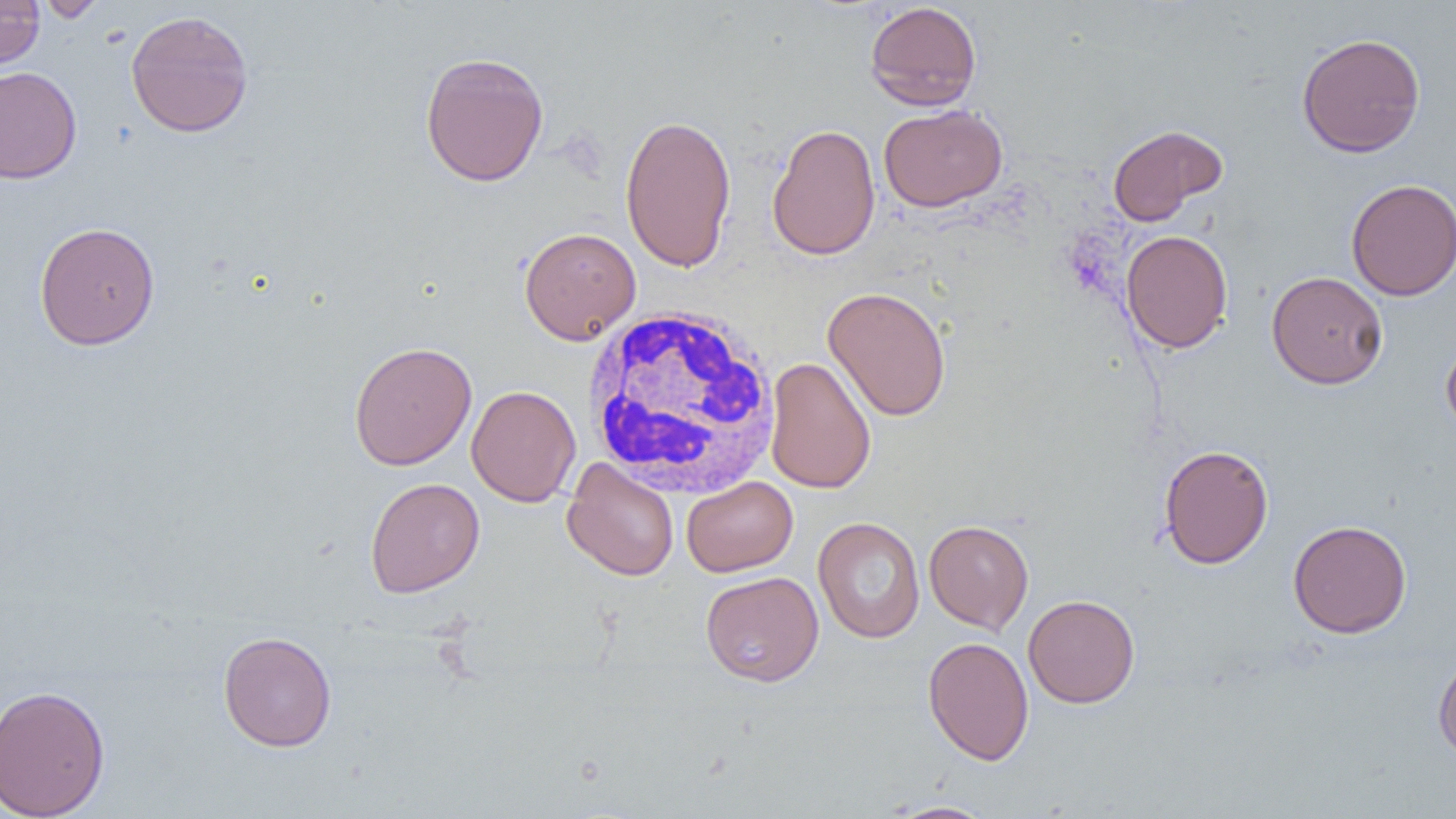
Summary:
  - Coordinate format: approximate bounding boxes as named x1/y1/x2/y2 corners in pixels
  - Uninfected red blood cell locations: (x1=0, y1=0, x2=45, y2=70), (x1=36, y1=0, x2=106, y2=22), (x1=864, y1=2, x2=983, y2=110), (x1=125, y1=10, x2=254, y2=138), (x1=1296, y1=32, x2=1426, y2=158), (x1=419, y1=51, x2=549, y2=187), (x1=0, y1=66, x2=82, y2=184), (x1=878, y1=104, x2=1007, y2=212), (x1=620, y1=112, x2=738, y2=273), (x1=767, y1=123, x2=881, y2=261), (x1=1107, y1=124, x2=1228, y2=226), (x1=1346, y1=178, x2=1456, y2=301), (x1=34, y1=221, x2=160, y2=350), (x1=519, y1=226, x2=641, y2=344), (x1=1120, y1=229, x2=1233, y2=353), (x1=1266, y1=271, x2=1388, y2=389), (x1=822, y1=286, x2=951, y2=422), (x1=1441, y1=338, x2=1456, y2=438), (x1=348, y1=341, x2=477, y2=470), (x1=765, y1=357, x2=876, y2=494), (x1=466, y1=385, x2=581, y2=507), (x1=1158, y1=443, x2=1273, y2=569), (x1=562, y1=458, x2=679, y2=581), (x1=681, y1=476, x2=798, y2=576), (x1=364, y1=477, x2=485, y2=598), (x1=813, y1=517, x2=925, y2=644), (x1=924, y1=519, x2=1034, y2=635), (x1=1287, y1=519, x2=1412, y2=638), (x1=700, y1=571, x2=824, y2=687), (x1=1023, y1=594, x2=1140, y2=708), (x1=218, y1=630, x2=337, y2=752), (x1=922, y1=636, x2=1034, y2=765), (x1=1433, y1=653, x2=1456, y2=763), (x1=0, y1=684, x2=111, y2=819), (x1=883, y1=800, x2=999, y2=818)
  - White blood cell locations: (x1=581, y1=305, x2=782, y2=499)
  - Slide-level diagnosis: no evidence of blood parasites
  - Magnification: 1000x
  - Modality: light microscopy
  - Field of view: single
  - Preparation: thin blood film
  - Image size: 1456×819 pixels